Report the malaria status of this cell.
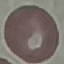

It is uninfected.

image type = cell patch, automatically extracted from a larger field of view and resized to 64 × 64 pixels
capture = smartphone camera at the microscope eyepiece
preparation = thin smear
stain = Giemsa